Report the malaria status of this cell.
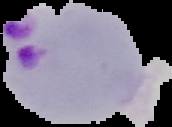

It is parasitized.

Image is 172×127 pixels. From a thin blood smear. The area outside the segmented cell region is set to black.